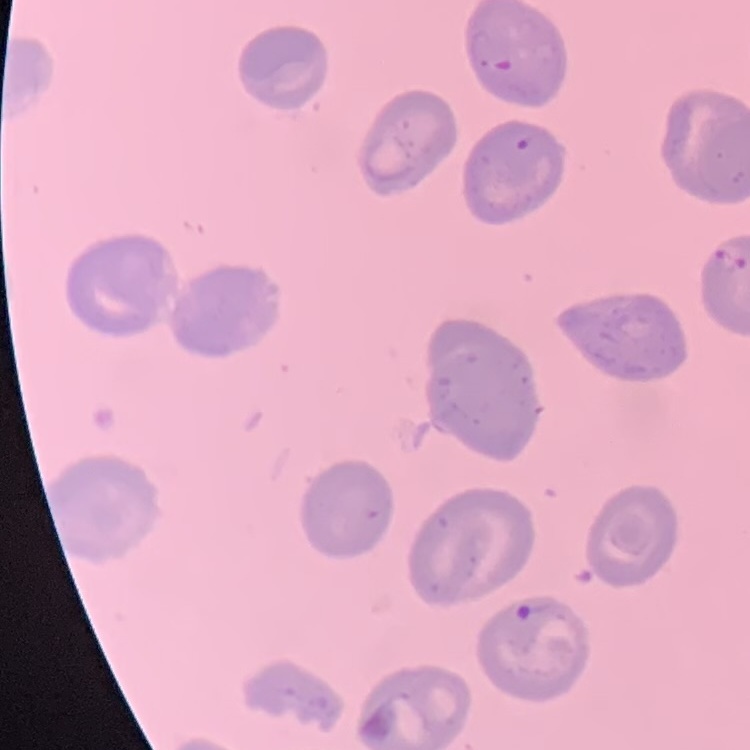

{
  "red_blood_cell_morphology": "no rouleaux formation",
  "preparation": "thin blood film",
  "stain": "Field's or Giemsa",
  "image_type": "one tile cut from a larger photomicrograph"
}